Outline each blood parasite and name the species.
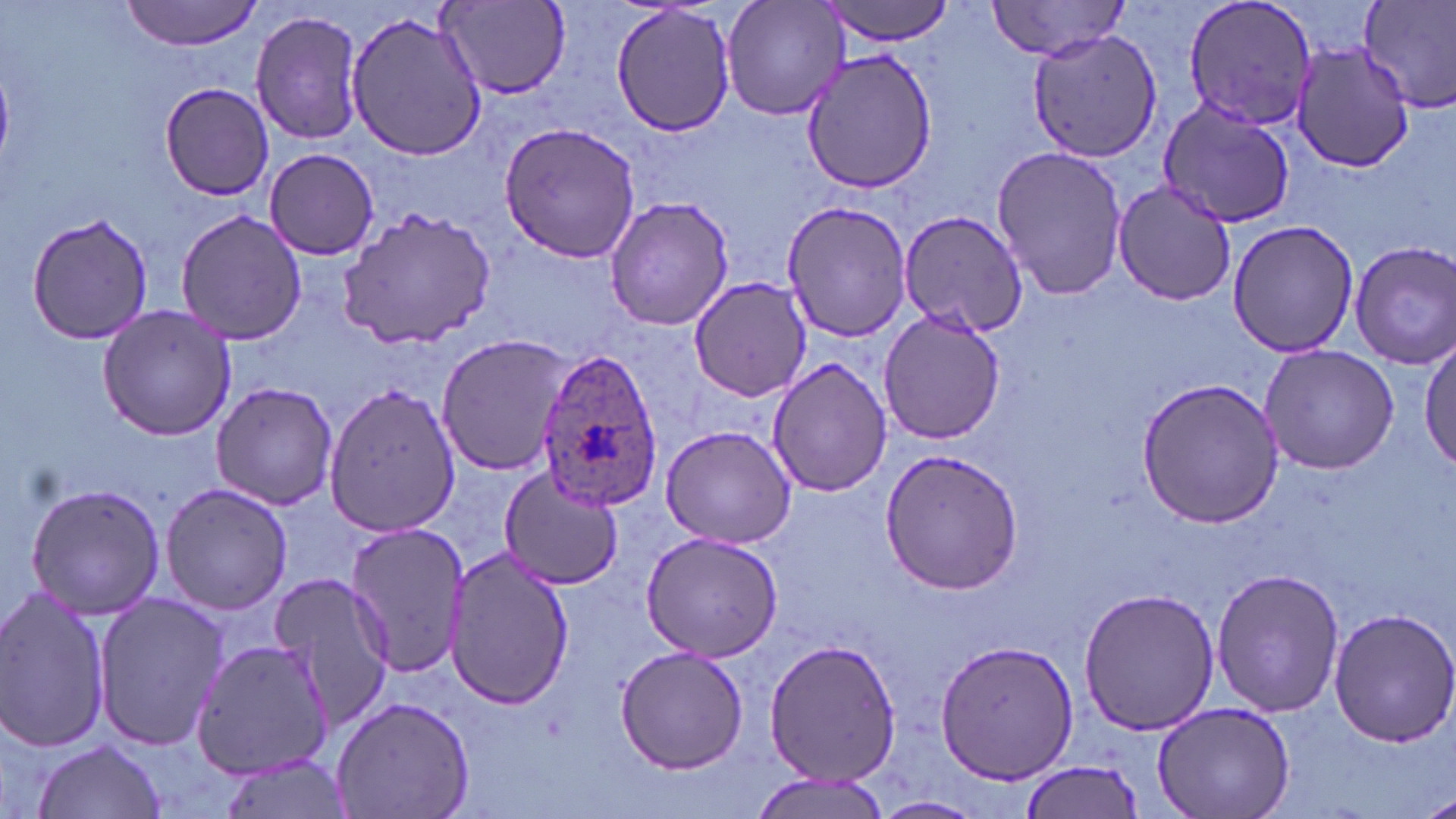

Approximate bounding boxes as (x1,y1)-(x2,y2) corner pairs in pixels.
Plasmodium ovale-infected red blood cells: (534,346)-(663,510).
No Plasmodium falciparum, Plasmodium malariae, Plasmodium vivax, Babesia divergens, or Trypanosoma brucei observed.

Summary:
  - Uninfected red blood cell locations: (119,0)-(266,50), (438,0)-(572,98), (722,0)-(848,121), (821,0)-(957,46), (983,0)-(1134,60), (1179,0)-(1320,134), (1360,0)-(1456,112), (610,3)-(737,139), (248,8)-(367,147), (345,8)-(489,164), (1029,30)-(1163,162), (1286,40)-(1418,173), (799,50)-(939,192), (159,82)-(274,200), (1156,98)-(1295,229), (499,120)-(642,263), (992,146)-(1130,301), (263,147)-(379,260), (1112,179)-(1240,306), (605,196)-(735,332), (780,199)-(914,343), (177,207)-(306,347), (335,208)-(498,349), (898,210)-(1029,335), (21,212)-(155,346), (1227,220)-(1360,358), (1351,241)-(1456,370), (688,277)-(811,401), (96,304)-(237,441), (879,309)-(1005,445), (1419,332)-(1455,475), (434,335)-(571,475), (1259,345)-(1399,474), (767,357)-(890,499), (1135,377)-(1284,528), (324,380)-(460,537), (209,382)-(338,510), (659,424)-(798,549), (879,448)-(1025,597), (497,468)-(623,591), (25,483)-(166,620), (160,483)-(292,617), (348,523)-(473,676), (640,532)-(785,661), (444,552)-(575,707), (1211,567)-(1345,717), (269,572)-(397,729), (0,587)-(112,755), (1078,587)-(1221,736), (91,591)-(227,753), (1328,608)-(1456,746), (762,636)-(901,787), (933,637)-(1079,786), (189,638)-(336,782), (613,642)-(748,776), (330,694)-(477,819), (1154,700)-(1296,818), (31,739)-(167,819), (213,753)-(353,819), (1017,759)-(1143,819), (748,773)-(892,819), (1418,787)-(1456,819), (872,795)-(984,818)
  - Slide-level diagnosis: Plasmodium ovale
  - Field of view: single
  - Preparation: thin blood smear
  - Modality: optical microscopy
  - Magnification: 1000x
  - Stain: May-Grünwald-Giemsa
  - Image size: 1456×819 pixels